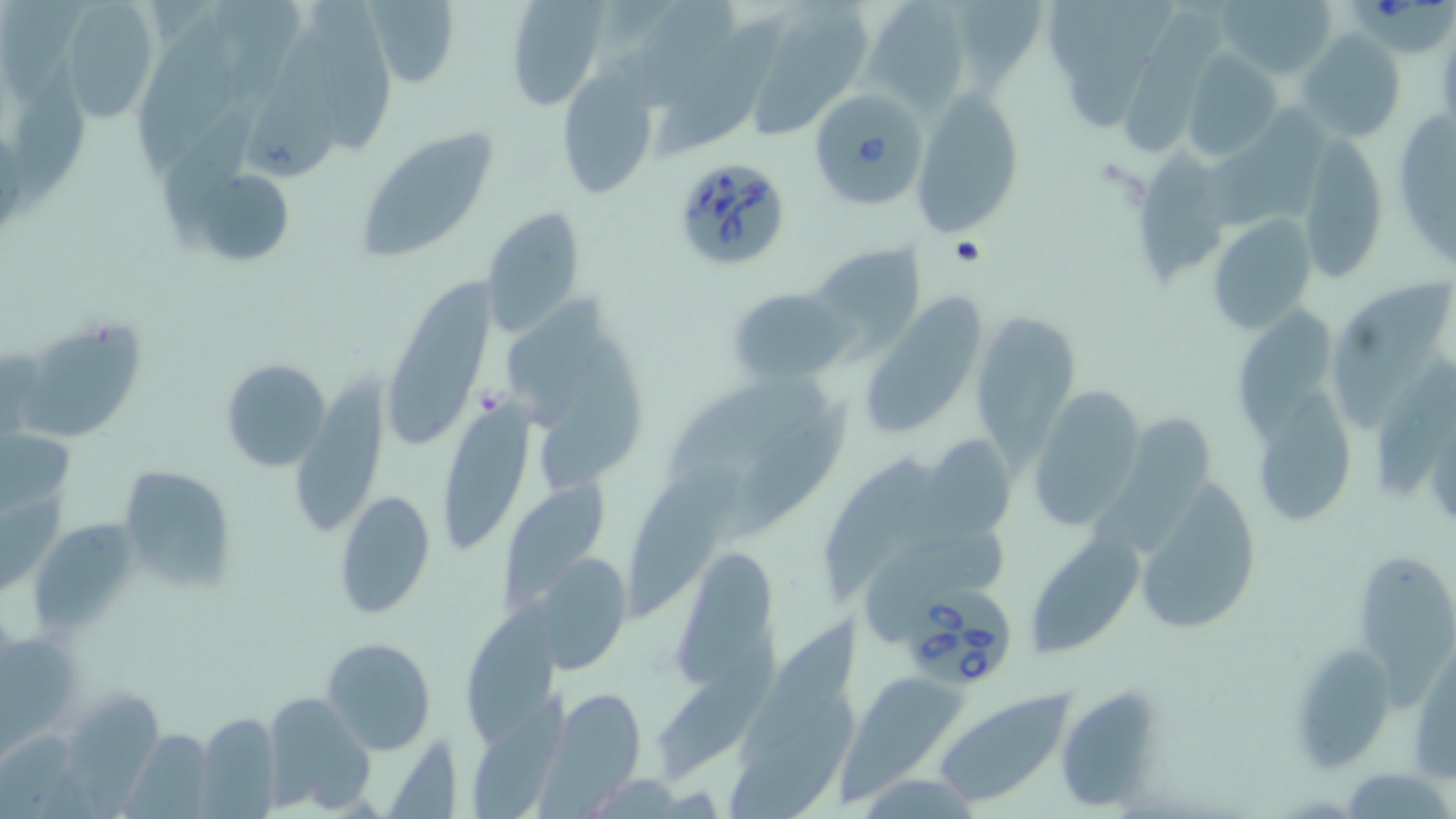
Approximate bounding boxes as (x1, y1, x2, y2) in pixels. Platelet locations: (475, 385, 511, 417). Babesia divergens-infected red blood cell locations: (1348, 0, 1454, 54), (804, 83, 934, 211), (668, 155, 793, 273), (903, 580, 1014, 687). Uninfected red blood cell locations: (58, 0, 165, 119), (364, 0, 459, 83), (503, 0, 607, 108), (636, 0, 741, 116), (867, 0, 964, 113), (951, 0, 1047, 93), (1067, 0, 1181, 134), (1216, 0, 1339, 80), (209, 1, 305, 108), (310, 2, 396, 155), (759, 3, 875, 137), (2, 6, 95, 110), (1122, 12, 1231, 156), (657, 19, 781, 161), (139, 22, 248, 172), (1298, 30, 1406, 143), (254, 36, 345, 179), (1181, 51, 1282, 162), (12, 56, 91, 218), (554, 70, 661, 201), (913, 90, 1026, 237), (1204, 101, 1338, 226), (1390, 102, 1456, 270), (165, 105, 263, 237), (356, 129, 495, 261), (1295, 133, 1388, 284), (1134, 152, 1228, 293), (188, 165, 296, 267), (480, 208, 589, 339), (1207, 216, 1317, 333), (809, 244, 925, 354), (386, 262, 501, 447), (1340, 276, 1452, 435), (866, 280, 998, 431), (729, 288, 854, 383), (1233, 297, 1338, 441), (974, 313, 1078, 459), (23, 317, 150, 446), (538, 339, 654, 491), (1376, 356, 1455, 494), (220, 358, 331, 469), (303, 358, 391, 525), (668, 377, 833, 493), (1027, 385, 1143, 530), (1259, 389, 1359, 528), (447, 396, 538, 550), (713, 400, 855, 542), (1096, 403, 1215, 558), (1, 426, 72, 531), (918, 430, 1019, 545), (818, 451, 948, 595), (621, 462, 747, 617), (116, 464, 234, 591), (495, 470, 614, 612), (1131, 472, 1264, 636), (336, 490, 436, 618), (33, 515, 144, 633), (869, 528, 1012, 642), (1028, 534, 1144, 662), (671, 542, 780, 685), (1356, 542, 1456, 708), (540, 551, 635, 673), (461, 600, 568, 742), (742, 616, 867, 766), (654, 635, 781, 784), (0, 637, 82, 754), (321, 637, 435, 755), (1286, 643, 1396, 771), (1411, 662, 1455, 780), (842, 678, 966, 809), (1064, 682, 1155, 809), (469, 688, 571, 819), (555, 688, 647, 797), (933, 688, 1075, 806), (70, 689, 167, 812), (260, 690, 375, 813), (728, 696, 860, 819), (194, 711, 282, 817), (0, 730, 80, 819), (127, 730, 215, 819), (390, 731, 458, 819), (1343, 767, 1452, 819). Slide-level diagnosis: Babesia divergens. Image is 1456×819 pixels. Thin blood smear. 1000x magnification. Single field of view. Light microscopy. May-Grünwald-Giemsa stain.